Locate every blood parasite and identify its species.
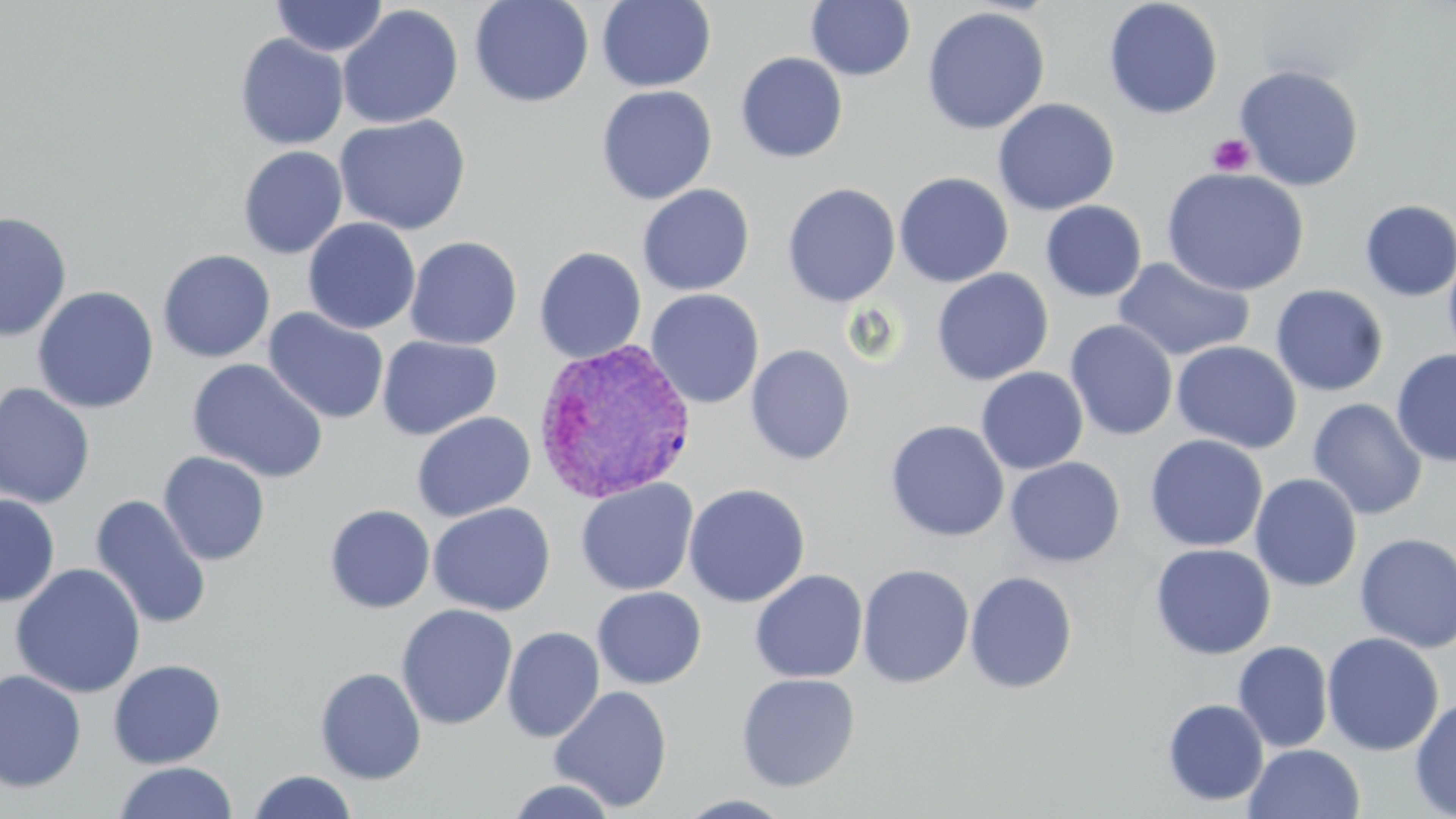
Approximate bounding boxes as (x1, y1, x2, y2) in pixels.
Plasmodium vivax-infected red blood cells: (532, 338, 697, 506).
No Plasmodium falciparum, Plasmodium ovale, Plasmodium malariae, Babesia divergens, or Trypanosoma brucei observed.

slide-level diagnosis = Plasmodium vivax
uninfected red blood cell locations = approximate bounding boxes as (x1, y1, x2, y2) in pixels: (271, 0, 388, 57), (470, 0, 594, 107), (805, 0, 916, 81), (1103, 0, 1224, 120), (596, 1, 717, 92), (338, 5, 463, 129), (922, 6, 1051, 135), (235, 33, 349, 150), (735, 51, 848, 163), (1234, 64, 1365, 191), (596, 85, 718, 205), (993, 97, 1120, 215), (334, 114, 471, 235), (238, 145, 348, 259), (1161, 167, 1310, 297), (893, 171, 1014, 287), (782, 183, 901, 307), (638, 184, 755, 296), (1359, 199, 1456, 302), (1041, 200, 1147, 302), (0, 211, 73, 342), (303, 217, 421, 334), (405, 236, 522, 350), (533, 246, 647, 363), (1442, 246, 1456, 366), (157, 249, 276, 362), (1113, 257, 1255, 363), (931, 268, 1054, 385), (1270, 284, 1389, 397), (31, 286, 159, 414), (645, 289, 764, 408), (263, 308, 390, 425), (1065, 319, 1178, 441), (376, 335, 502, 440), (1171, 340, 1303, 454), (745, 344, 856, 465), (1391, 348, 1456, 468), (186, 359, 329, 483), (976, 367, 1088, 474), (0, 382, 96, 509), (1307, 397, 1428, 520), (412, 411, 536, 522), (885, 420, 1009, 542), (1145, 435, 1268, 552), (158, 451, 271, 566), (1004, 457, 1125, 568), (1249, 473, 1363, 592), (575, 478, 699, 596), (683, 483, 810, 608), (0, 494, 60, 607), (89, 494, 212, 631), (428, 502, 555, 616), (324, 504, 435, 613), (1354, 533, 1456, 653), (1149, 543, 1277, 660), (10, 562, 147, 699), (856, 564, 975, 689), (750, 569, 868, 684), (965, 571, 1079, 694), (591, 587, 707, 689), (396, 604, 518, 730), (502, 626, 604, 743), (1321, 632, 1444, 756), (1233, 641, 1333, 752), (107, 659, 226, 769), (315, 667, 427, 784), (0, 669, 87, 793), (736, 673, 860, 791), (548, 685, 673, 813), (1410, 696, 1456, 818), (1162, 698, 1269, 806), (1244, 743, 1366, 819), (112, 761, 237, 819), (247, 769, 358, 819), (504, 778, 619, 818), (675, 793, 797, 818)
field of view = one of a larger specimen
modality = optical microscopy
preparation = thin blood smear
platelet locations = approximate bounding boxes as (x1, y1, x2, y2) in pixels: (1207, 133, 1255, 177)
image size = 1456×819 pixels
stain = May-Grünwald-Giemsa
magnification = 1000x